Classify this cell by malaria status.
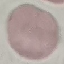

Uninfected.

Summary:
  - Capture: smartphone camera at the microscope eyepiece
  - Image type: cell patch, automatically extracted from a larger field of view and resized to 64 × 64 pixels
  - Preparation: thin blood smear
  - Stain: Giemsa